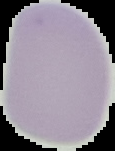

image size = 115×151 pixels
preparation = thin blood smear
result = no Plasmodium parasites detected
image type = cell region segmented out of the field of view; surrounding area masked to black